Name the cell type shown.
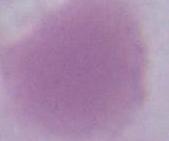

This is an erythrocyte.

modality = photomicrograph
magnification = 1000x